State which parasite is depicted.
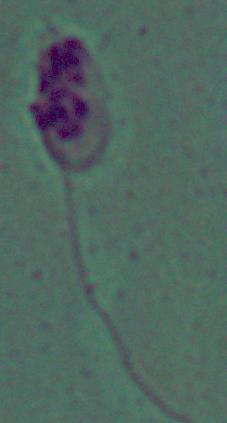
Leishmania.

magnification: 1000x
modality: photomicrograph